Give the extent of all uninfected red blood cells.
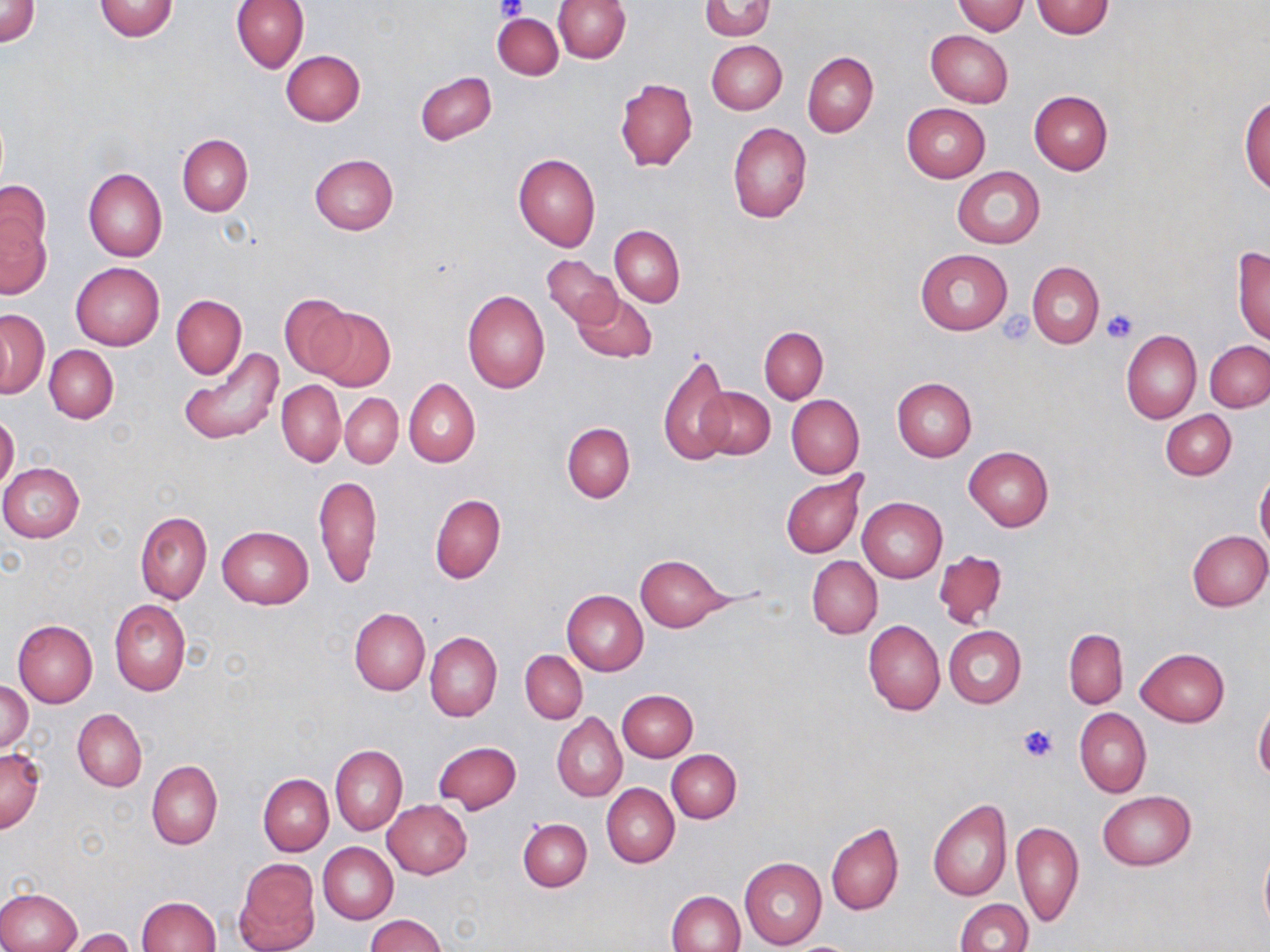

Approximate bounding boxes as (x1, y1, x2, y2) in pixels.
Uninfected red blood cells: (1, 0, 40, 46), (232, 0, 309, 73), (552, 0, 631, 62), (94, 1, 179, 41), (951, 1, 1027, 35), (1032, 1, 1114, 38), (699, 2, 774, 40), (496, 7, 625, 69), (493, 12, 563, 79), (926, 30, 1014, 107), (707, 40, 787, 114), (280, 50, 365, 126), (802, 52, 878, 137), (416, 71, 497, 145), (615, 78, 698, 171), (1028, 90, 1113, 174), (1240, 94, 1269, 195), (901, 104, 991, 183), (727, 122, 811, 223), (178, 134, 253, 217), (309, 153, 398, 234), (512, 153, 601, 251), (953, 166, 1045, 248), (82, 169, 166, 262), (0, 181, 50, 260), (1, 217, 51, 298), (609, 225, 685, 306), (1232, 246, 1270, 344), (916, 248, 1012, 336), (542, 254, 621, 327), (71, 262, 165, 350), (1028, 262, 1104, 348), (572, 289, 657, 363), (461, 290, 550, 393), (279, 294, 358, 379), (171, 295, 247, 379), (309, 306, 396, 392), (0, 310, 49, 398), (759, 326, 828, 404), (1122, 330, 1202, 424), (1204, 339, 1270, 413), (45, 345, 118, 422), (176, 345, 286, 445), (658, 351, 732, 468), (404, 378, 480, 467), (892, 378, 976, 462), (276, 380, 345, 465), (696, 385, 775, 461), (340, 392, 403, 470), (787, 395, 864, 478), (1161, 410, 1236, 479), (0, 412, 19, 493), (562, 423, 635, 503), (964, 445, 1054, 531), (0, 463, 84, 542), (782, 472, 867, 558), (1255, 472, 1270, 552), (314, 474, 382, 590), (431, 494, 506, 583), (857, 497, 947, 582), (135, 511, 211, 604), (217, 526, 312, 608), (1186, 530, 1270, 612), (932, 549, 1009, 630), (635, 555, 734, 631), (807, 557, 883, 638), (562, 590, 648, 675), (110, 599, 190, 695), (350, 608, 430, 696), (12, 619, 98, 706), (863, 619, 945, 716), (942, 625, 1026, 708), (1064, 629, 1128, 708), (425, 632, 502, 722), (1135, 648, 1229, 727), (521, 650, 587, 723), (0, 680, 32, 755), (616, 689, 698, 761), (1254, 701, 1270, 784), (1076, 708, 1151, 797), (73, 709, 146, 792), (552, 713, 627, 802), (434, 740, 521, 813), (330, 745, 407, 835), (0, 746, 45, 834), (665, 749, 742, 823), (147, 760, 222, 849), (258, 773, 333, 855), (602, 784, 679, 868), (1099, 791, 1195, 870), (928, 799, 1013, 901), (383, 800, 473, 879), (518, 817, 592, 892), (1012, 820, 1083, 929), (826, 823, 904, 916), (319, 842, 398, 924), (1259, 842, 1270, 935), (740, 857, 826, 950), (235, 858, 319, 951), (0, 888, 82, 952), (667, 890, 745, 952), (137, 896, 221, 951), (955, 899, 1032, 952), (367, 914, 445, 951), (63, 928, 136, 952).

slide-level diagnosis = negative for blood parasites
preparation = thin blood smear
modality = light microscopy
magnification = 1000x
stain = May-Grünwald-Giemsa
platelet locations = approximate bounding boxes as (x1, y1, x2, y2) in pixels: (495, 0, 527, 19), (1102, 310, 1138, 344), (1001, 311, 1037, 345), (1017, 724, 1057, 763)
image size = 1270×952 pixels
field of view = single